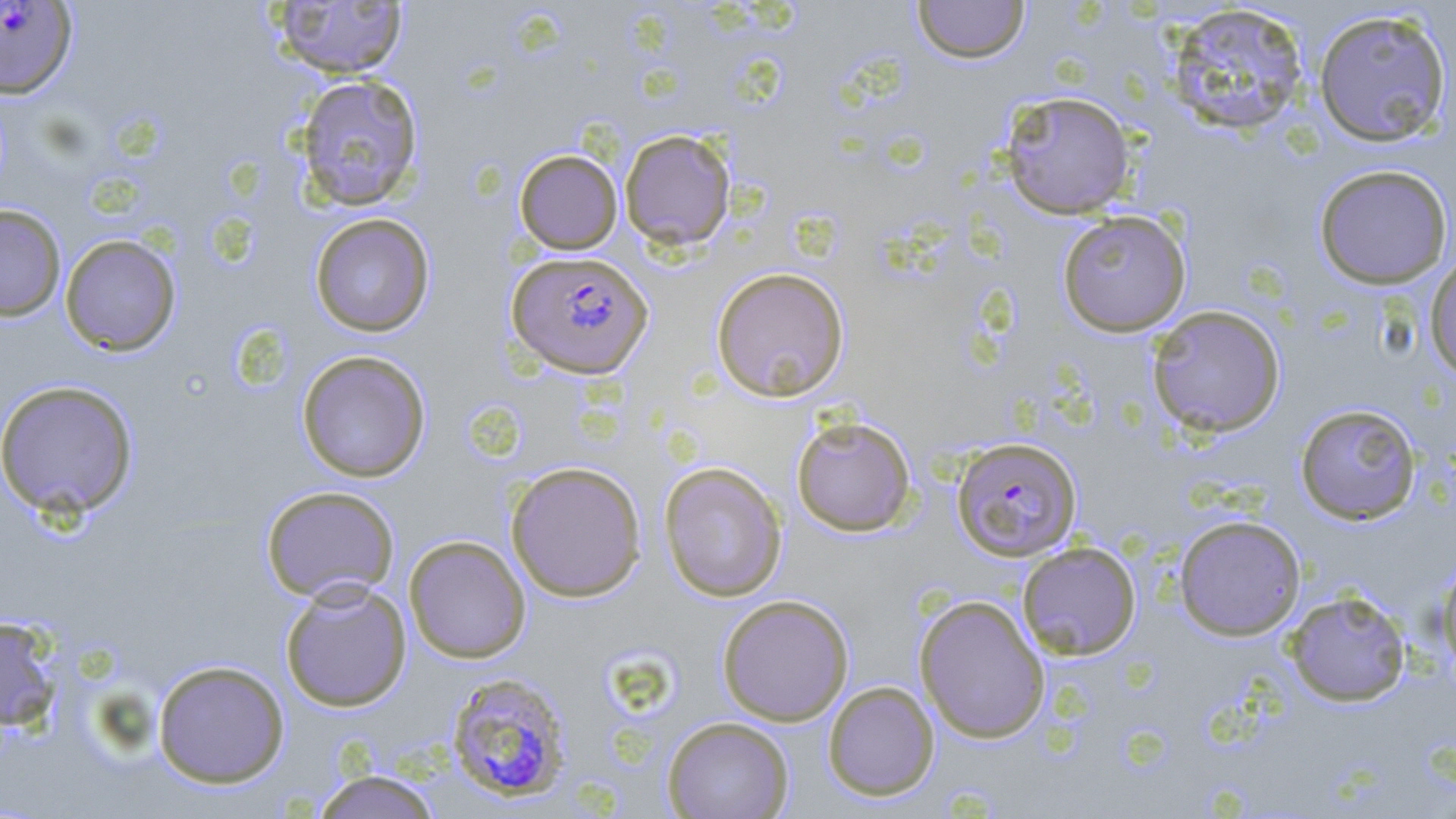 Approximate bounding boxes as [x1, y1, x2, y2] in pixels. Uninfected red blood cell locations: [269, 0, 409, 79], [912, 0, 1030, 64], [1165, 4, 1310, 136], [1312, 7, 1453, 148], [294, 74, 424, 211], [999, 90, 1136, 219], [619, 129, 737, 251], [514, 149, 623, 254], [1313, 164, 1454, 289], [0, 204, 67, 321], [1056, 210, 1192, 337], [309, 213, 435, 337], [59, 234, 182, 356], [1423, 251, 1456, 382], [711, 266, 850, 402], [1146, 304, 1286, 438], [296, 350, 431, 483], [0, 379, 139, 520], [1294, 402, 1422, 525], [791, 415, 917, 537], [505, 460, 647, 602], [659, 461, 787, 602], [260, 485, 401, 603], [1174, 514, 1306, 640], [404, 535, 531, 663], [1016, 542, 1142, 660], [1435, 555, 1456, 684], [279, 578, 412, 712], [1284, 590, 1411, 707], [717, 594, 854, 726], [914, 594, 1050, 744], [0, 615, 63, 731], [152, 659, 290, 788], [823, 681, 940, 801], [662, 716, 794, 819], [309, 769, 445, 819]. Plasmodium falciparum-infected red blood cell locations: [0, 1, 77, 99], [507, 250, 654, 379], [951, 437, 1082, 561], [444, 671, 574, 803]. Slide-level diagnosis: Plasmodium falciparum. 1000x magnification. Image is 1456×819 pixels. Thin blood smear. Optical microscopy. May-Grünwald-Giemsa stain. Single field of view.